Name the parasite shown.
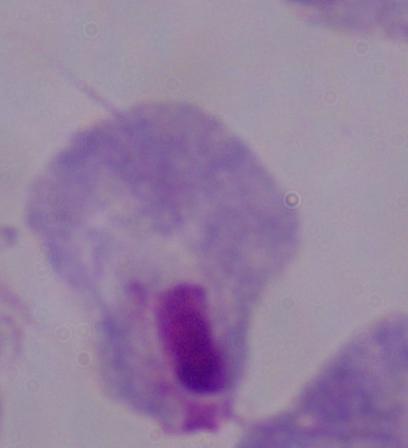

A trichomonad.

modality = photomicrograph
magnification = 1000x